Assess the morphology of the erythrocytes.
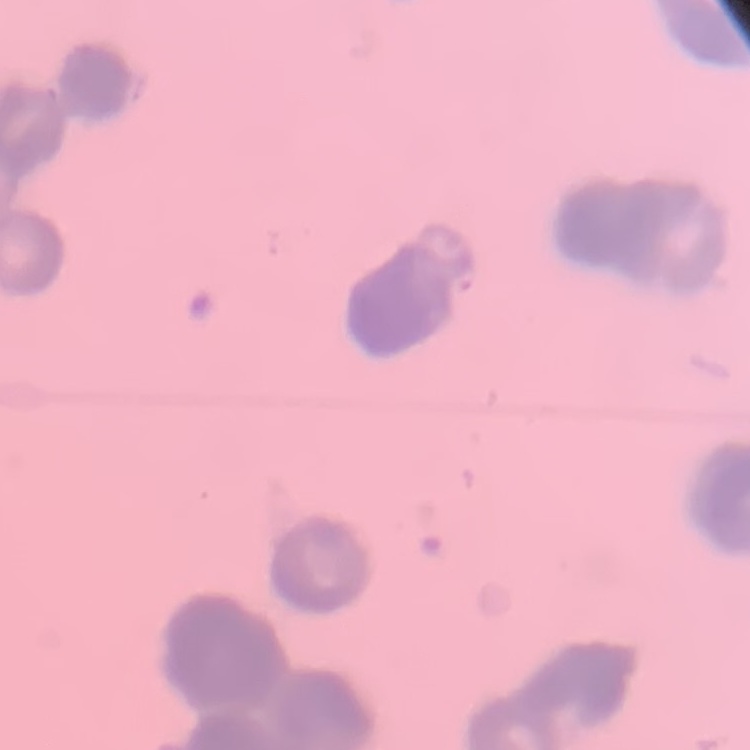

They show rouleaux formation.

stain = Field's or Giemsa
image type = square crop of a larger photomicrograph
preparation = thin blood smear